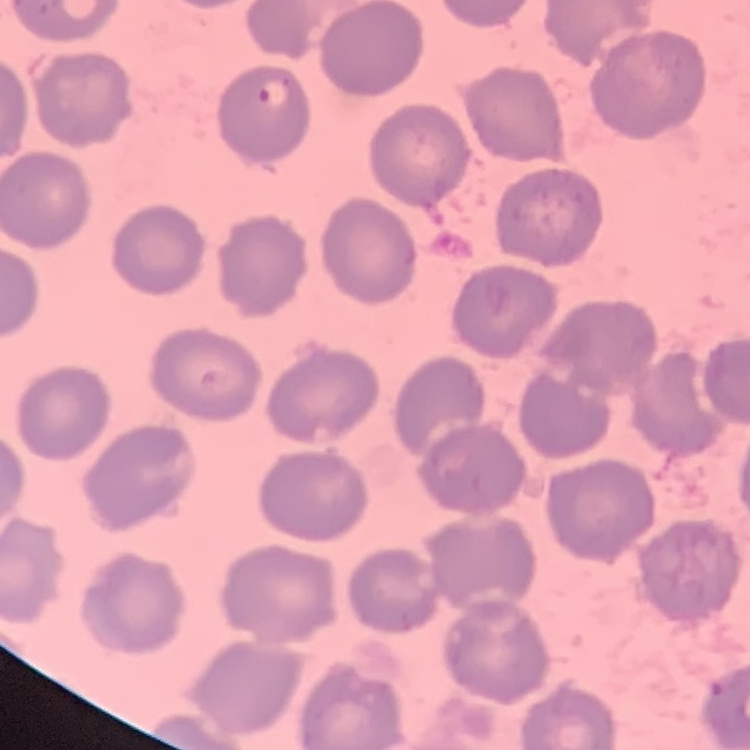

The erythrocytes exhibit no rouleaux formation. Square crop of a larger photomicrograph. Thin blood smear. Field's or Giemsa stain.